Outline each Plasmodium vivax-infected red blood cell.
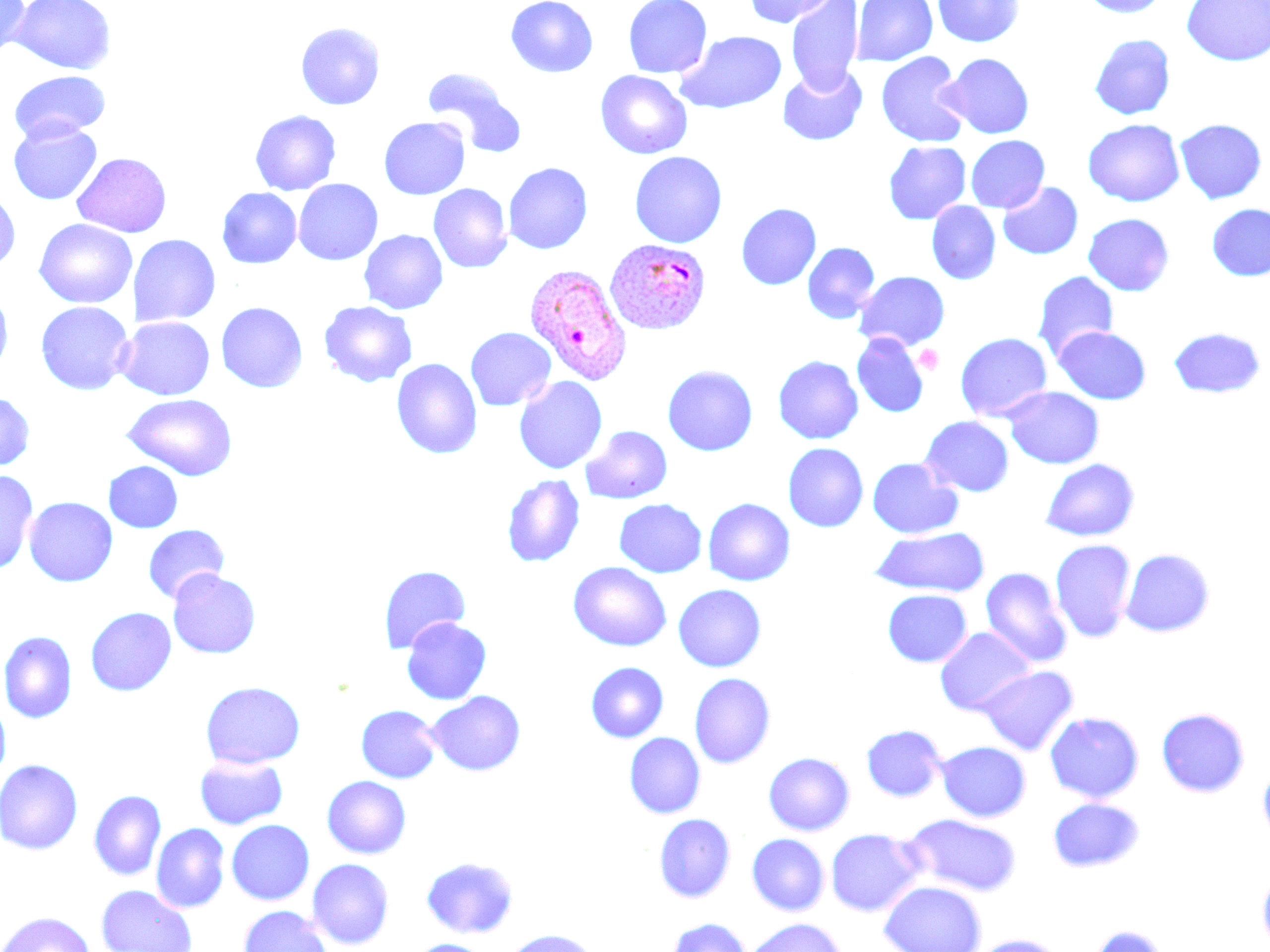
Approximate bounding boxes as named x1/y1/x2/y2 corners in pixels.
Plasmodium vivax-infected red blood cells: (x1=604, y1=237, x2=712, y2=335), (x1=524, y1=263, x2=634, y2=386).

slide-level diagnosis = Plasmodium vivax
platelet locations = approximate bounding boxes as named x1/y1/x2/y2 corners in pixels: (x1=914, y1=344, x2=944, y2=374)
stain = May-Grünwald-Giemsa
image size = 1270×952 pixels
preparation = thin blood smear
modality = light microscopy
uninfected red blood cell locations = approximate bounding boxes as named x1/y1/x2/y2 corners in pixels: (x1=0, y1=0, x2=31, y2=62), (x1=10, y1=0, x2=116, y2=74), (x1=506, y1=0, x2=598, y2=78), (x1=623, y1=0, x2=712, y2=79), (x1=742, y1=0, x2=838, y2=28), (x1=786, y1=0, x2=863, y2=93), (x1=853, y1=0, x2=937, y2=66), (x1=932, y1=0, x2=1025, y2=47), (x1=1080, y1=0, x2=1169, y2=17), (x1=1182, y1=0, x2=1269, y2=66), (x1=295, y1=22, x2=385, y2=110), (x1=676, y1=31, x2=787, y2=114), (x1=1090, y1=34, x2=1175, y2=120), (x1=876, y1=52, x2=969, y2=148), (x1=940, y1=53, x2=1034, y2=139), (x1=777, y1=65, x2=867, y2=146), (x1=423, y1=69, x2=526, y2=157), (x1=595, y1=70, x2=693, y2=159), (x1=9, y1=71, x2=110, y2=141), (x1=250, y1=110, x2=341, y2=195), (x1=378, y1=116, x2=470, y2=200), (x1=8, y1=119, x2=103, y2=205), (x1=1083, y1=119, x2=1185, y2=207), (x1=1174, y1=119, x2=1266, y2=204), (x1=966, y1=135, x2=1050, y2=213), (x1=883, y1=141, x2=971, y2=225), (x1=629, y1=151, x2=727, y2=248), (x1=72, y1=152, x2=172, y2=237), (x1=503, y1=162, x2=593, y2=254), (x1=293, y1=179, x2=383, y2=265), (x1=998, y1=182, x2=1083, y2=259), (x1=428, y1=183, x2=513, y2=273), (x1=217, y1=187, x2=302, y2=268), (x1=0, y1=189, x2=20, y2=271), (x1=926, y1=201, x2=1001, y2=285), (x1=736, y1=203, x2=821, y2=289), (x1=1207, y1=204, x2=1270, y2=281), (x1=1083, y1=213, x2=1175, y2=296), (x1=34, y1=218, x2=137, y2=308), (x1=359, y1=229, x2=447, y2=314), (x1=130, y1=234, x2=220, y2=327), (x1=803, y1=242, x2=880, y2=324), (x1=855, y1=271, x2=950, y2=351), (x1=1032, y1=271, x2=1118, y2=362), (x1=0, y1=288, x2=14, y2=375), (x1=319, y1=300, x2=417, y2=387), (x1=35, y1=301, x2=134, y2=395), (x1=216, y1=301, x2=308, y2=393), (x1=116, y1=316, x2=215, y2=400), (x1=1053, y1=326, x2=1151, y2=404), (x1=1168, y1=326, x2=1267, y2=398), (x1=465, y1=327, x2=556, y2=411), (x1=955, y1=332, x2=1052, y2=422), (x1=852, y1=333, x2=928, y2=417), (x1=773, y1=355, x2=863, y2=444), (x1=391, y1=358, x2=482, y2=459), (x1=662, y1=364, x2=758, y2=456), (x1=513, y1=376, x2=608, y2=474), (x1=1003, y1=387, x2=1104, y2=469), (x1=0, y1=391, x2=35, y2=471), (x1=121, y1=394, x2=238, y2=481), (x1=919, y1=416, x2=1014, y2=497), (x1=580, y1=425, x2=672, y2=504), (x1=783, y1=443, x2=869, y2=532), (x1=867, y1=457, x2=962, y2=539), (x1=1040, y1=458, x2=1140, y2=542), (x1=103, y1=461, x2=182, y2=533), (x1=0, y1=470, x2=38, y2=575), (x1=502, y1=475, x2=585, y2=567), (x1=24, y1=496, x2=118, y2=586), (x1=702, y1=498, x2=795, y2=586), (x1=614, y1=499, x2=707, y2=578), (x1=142, y1=524, x2=230, y2=604), (x1=870, y1=527, x2=990, y2=597), (x1=1049, y1=538, x2=1137, y2=643), (x1=1120, y1=548, x2=1216, y2=637), (x1=568, y1=562, x2=672, y2=651), (x1=378, y1=565, x2=471, y2=652), (x1=980, y1=567, x2=1072, y2=668), (x1=167, y1=569, x2=261, y2=659), (x1=673, y1=584, x2=766, y2=672), (x1=678, y1=585, x2=770, y2=765), (x1=883, y1=589, x2=972, y2=667), (x1=85, y1=607, x2=176, y2=696), (x1=401, y1=617, x2=491, y2=705), (x1=934, y1=627, x2=1036, y2=716), (x1=0, y1=631, x2=77, y2=723), (x1=585, y1=662, x2=669, y2=742), (x1=975, y1=665, x2=1079, y2=755), (x1=689, y1=673, x2=775, y2=769), (x1=200, y1=681, x2=305, y2=769), (x1=425, y1=691, x2=525, y2=776), (x1=0, y1=698, x2=11, y2=784), (x1=355, y1=704, x2=441, y2=783), (x1=1156, y1=707, x2=1250, y2=797), (x1=1044, y1=711, x2=1144, y2=803), (x1=861, y1=724, x2=947, y2=801), (x1=624, y1=732, x2=705, y2=818), (x1=936, y1=741, x2=1031, y2=822), (x1=763, y1=752, x2=855, y2=836), (x1=194, y1=755, x2=288, y2=830), (x1=0, y1=759, x2=83, y2=854), (x1=1258, y1=761, x2=1270, y2=847), (x1=322, y1=775, x2=411, y2=859), (x1=89, y1=790, x2=166, y2=881), (x1=1048, y1=797, x2=1144, y2=872), (x1=654, y1=813, x2=735, y2=902), (x1=904, y1=814, x2=1022, y2=897), (x1=226, y1=819, x2=314, y2=905), (x1=151, y1=823, x2=230, y2=913), (x1=825, y1=829, x2=924, y2=916), (x1=747, y1=833, x2=830, y2=916), (x1=422, y1=856, x2=518, y2=938), (x1=307, y1=858, x2=394, y2=949), (x1=1257, y1=868, x2=1270, y2=951), (x1=879, y1=880, x2=986, y2=952), (x1=96, y1=884, x2=197, y2=952), (x1=238, y1=905, x2=333, y2=952), (x1=0, y1=911, x2=95, y2=952), (x1=665, y1=917, x2=752, y2=952), (x1=743, y1=917, x2=845, y2=952), (x1=1088, y1=925, x2=1172, y2=952), (x1=500, y1=929, x2=603, y2=952), (x1=968, y1=934, x2=1067, y2=952), (x1=408, y1=938, x2=493, y2=952)
magnification = 1000x
field of view = single